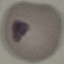
Result: no malaria parasites detected. Photographed with a smartphone camera at the microscope eyepiece. Thin blood film. Giemsa-stained preparation. Cell patch, automatically extracted from a larger field of view and resized to 64 × 64 pixels.